Name the blood parasite species.
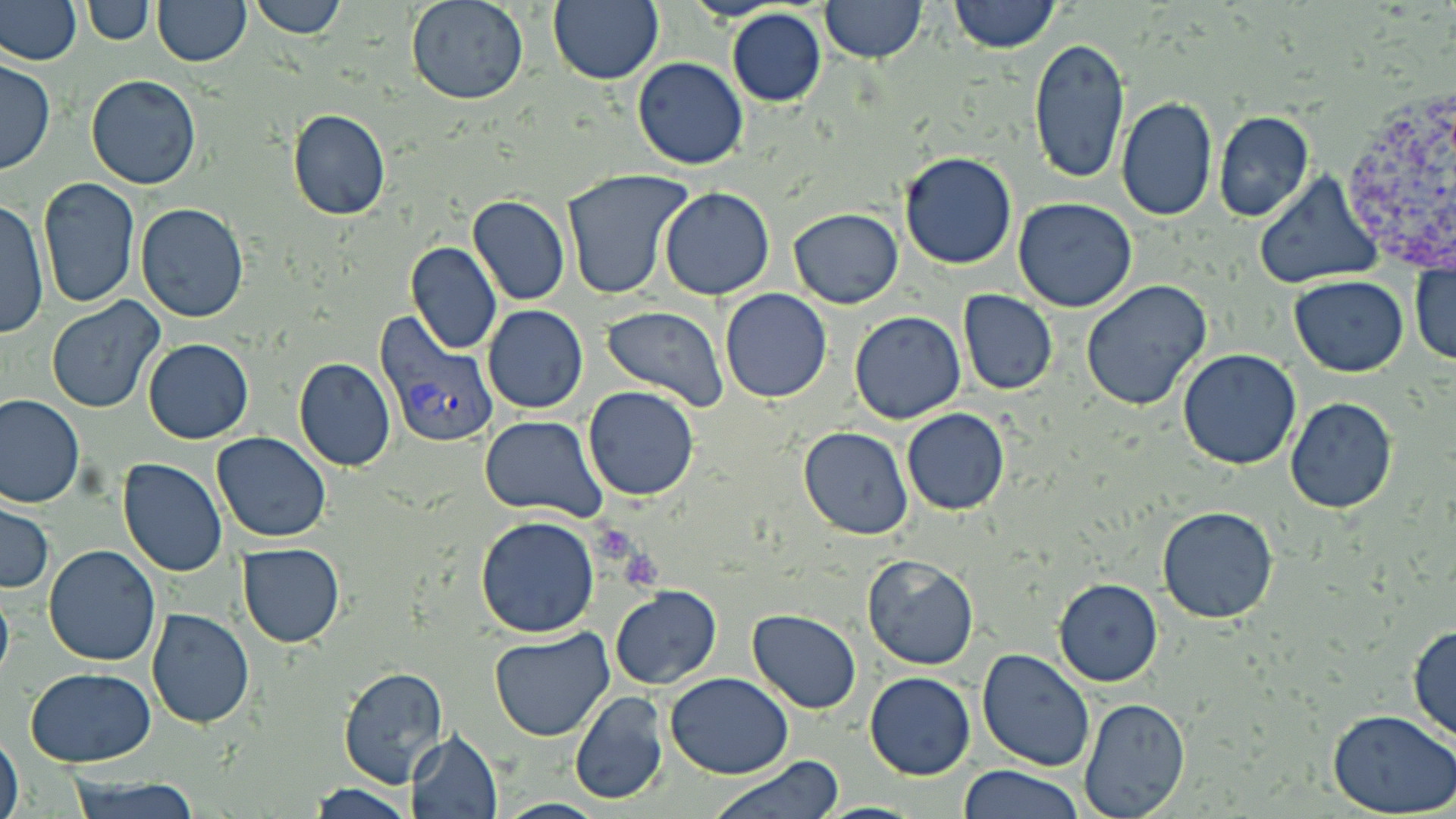
Plasmodium vivax.

Summary:
  - Coordinate format: approximate bounding boxes as (x1,y1)-(x2,y2) corner pairs in pixels
  - Uninfected red blood cell locations: (1,0)-(83,64), (153,0)-(250,66), (247,0)-(347,39), (406,0)-(528,105), (821,0)-(926,62), (949,0)-(1059,52), (82,1)-(156,46), (547,2)-(664,85), (728,8)-(827,107), (1026,36)-(1132,187), (630,57)-(748,170), (0,58)-(55,175), (84,75)-(201,191), (1114,97)-(1219,221), (286,108)-(392,221), (1214,110)-(1314,222), (898,152)-(1018,270), (560,169)-(695,300), (1252,172)-(1384,289), (37,177)-(140,309), (659,187)-(775,300), (467,196)-(570,306), (1013,198)-(1140,313), (1,199)-(50,341), (134,202)-(250,322), (788,207)-(904,308), (405,242)-(501,354), (1411,259)-(1456,369), (1289,276)-(1409,376), (1082,280)-(1213,412), (719,288)-(832,403), (957,290)-(1058,395), (46,298)-(164,414), (483,306)-(589,414), (601,306)-(730,413), (847,312)-(964,425), (142,338)-(254,445), (1177,348)-(1301,471), (292,358)-(397,471), (583,386)-(699,501), (1,394)-(84,507), (1284,397)-(1398,514), (900,408)-(1010,515), (479,416)-(605,521), (798,426)-(913,539), (212,432)-(332,542), (117,457)-(227,577), (0,502)-(53,593), (1156,505)-(1281,624), (475,516)-(600,637), (237,543)-(345,647), (43,544)-(161,665), (861,556)-(979,670), (1054,578)-(1163,687), (0,581)-(15,694), (610,585)-(722,689), (147,608)-(254,729), (748,609)-(861,713), (1407,623)-(1456,743), (489,630)-(615,742), (976,647)-(1096,770), (338,666)-(448,787), (25,667)-(156,768), (865,671)-(976,780), (665,673)-(794,777), (568,692)-(669,806), (1079,697)-(1189,816), (1328,710)-(1456,816), (1,729)-(24,819), (405,730)-(503,818), (708,757)-(845,819), (955,765)-(1086,819), (63,773)-(204,818), (306,782)-(412,818)
  - Platelet locations: (590,525)-(643,563), (626,553)-(664,592)
  - Plasmodium vivax-infected red blood cell locations: (375,314)-(498,449)
  - Magnification: 1000x
  - Modality: light microscopy
  - Field of view: single
  - Image size: 1456×819 pixels
  - Preparation: thin blood smear
  - Stain: May-Grünwald-Giemsa